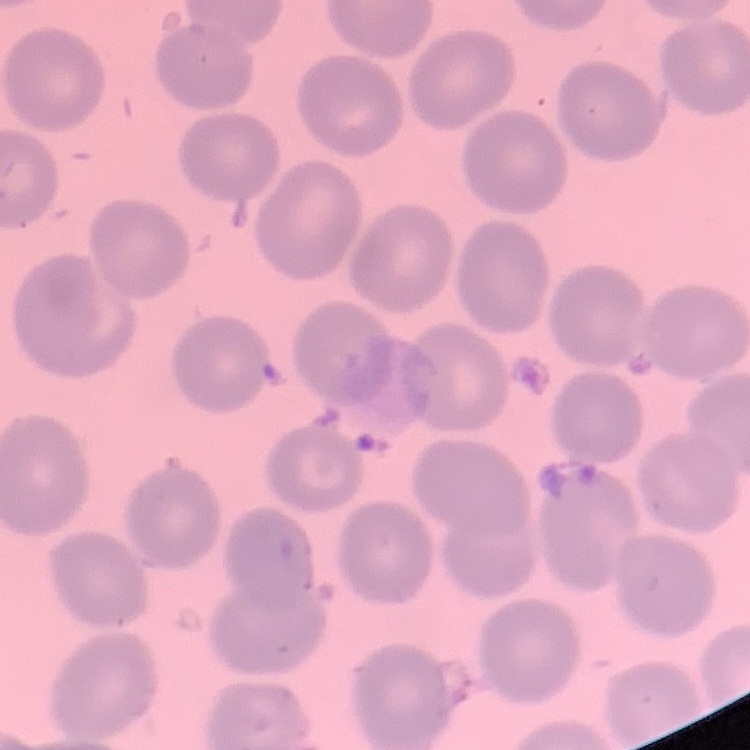

Summary:
  - Erythrocyte morphology: no rouleaux formation
  - Stain: Field's or Giemsa
  - Preparation: thin peripheral smear
  - Image type: one tile cut from a larger photomicrograph